Describe the morphology of the erythrocytes.
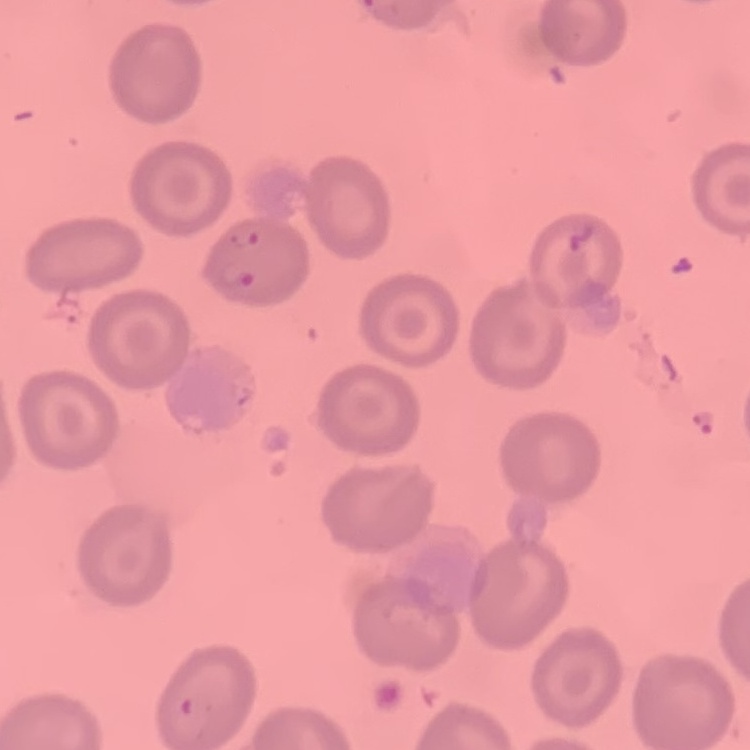
They show no rouleaux formation.

{
  "image_type": "square crop of a larger photomicrograph",
  "stain": "Field's or Giemsa",
  "preparation": "thin blood smear"
}